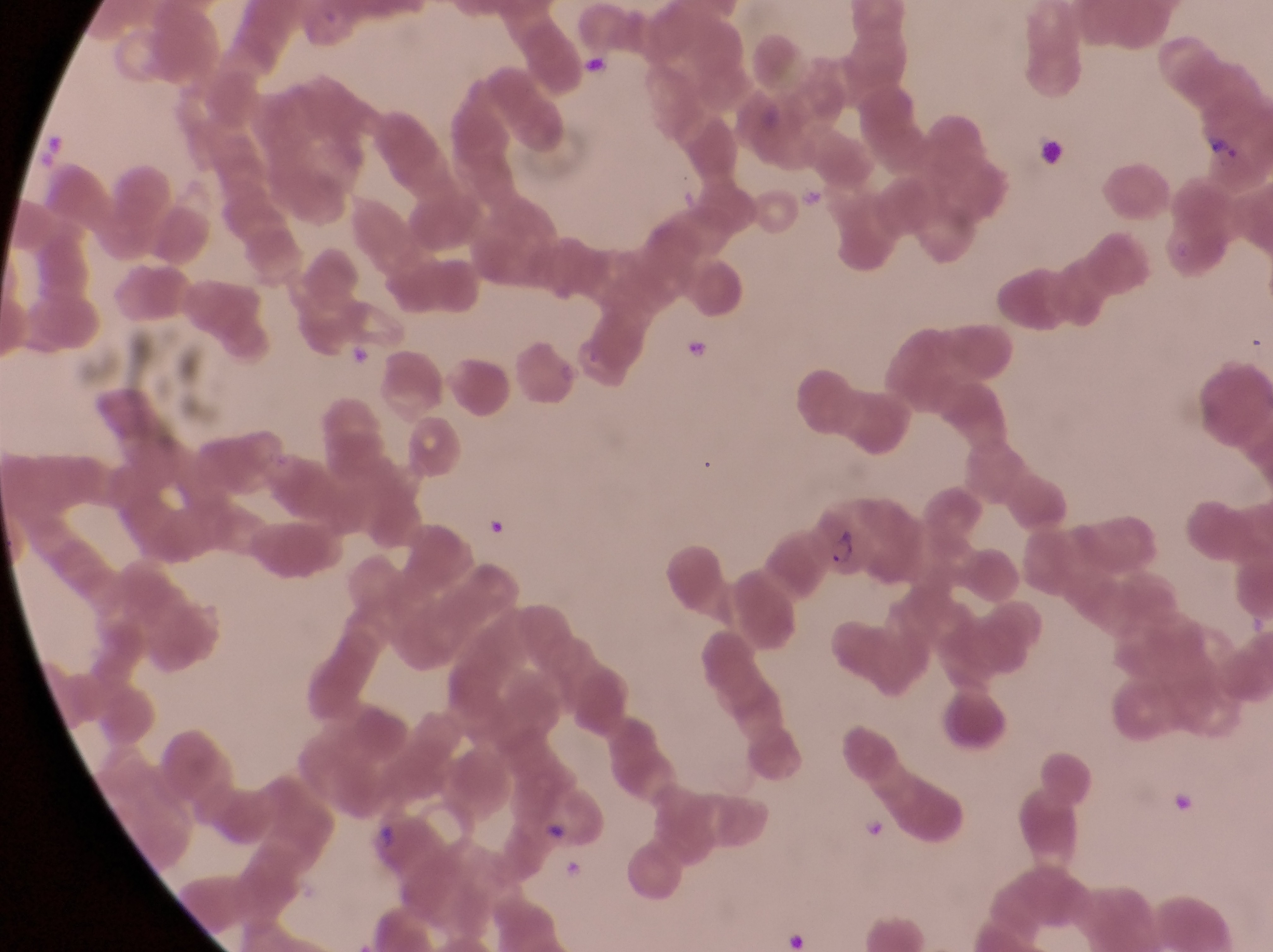

Approximate bounding boxes as (left, top, right, bottom) in pixels. Artifact (platelet-like body, stain precipitate, or debris) locations: (796, 182, 831, 210), (681, 337, 713, 369), (350, 344, 377, 374). Trophozoite locations: (1193, 118, 1251, 181). Parasitised red blood cell locations: (806, 505, 880, 582). Collected in Uganda. Image is 1273×952 pixels. Single field of view. Captured by a smartphone held over the eyepiece of an Olympus CX-23 microscope. Magnification of 1000x. Thin blood film.